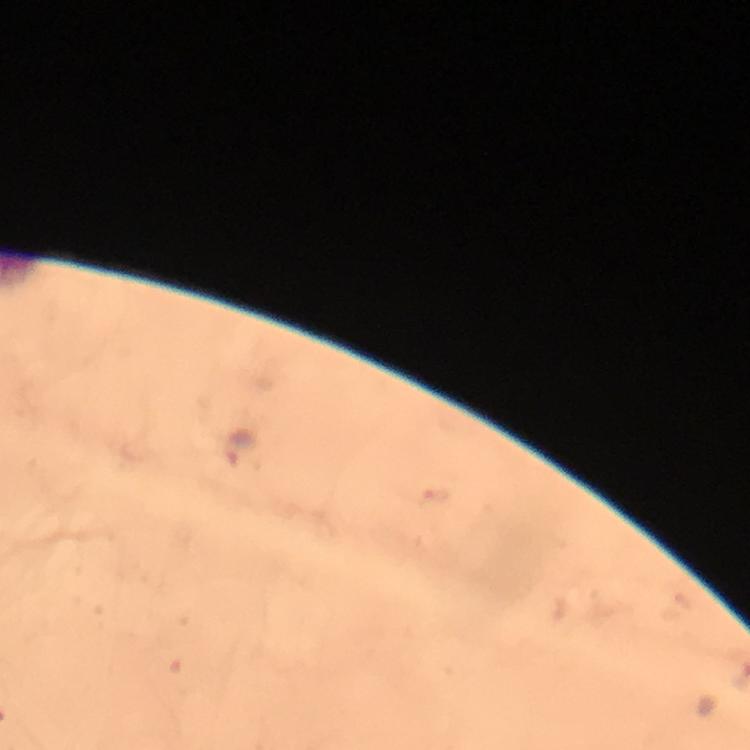

Approximate centers as (x, y) in pixels. Plasmodium parasite locations: (241, 448). Cropped region of a single field of view. Giemsa-stained preparation. Thick blood smear. Image is 750×750 pixels. 100x magnification. Photographed with a smartphone mounted on the microscope. Immersion oil was used. From a diagnostic examination for malaria.